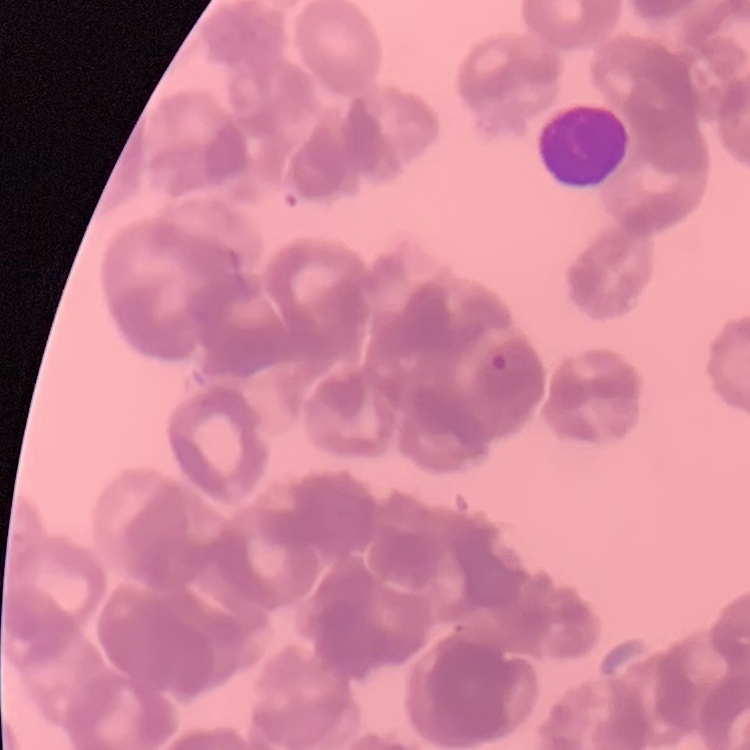

Summary:
  - Red blood cell morphology: rouleaux formation
  - Preparation: thin peripheral smear
  - Stain: Field's or Giemsa
  - Image type: one tile cut from a larger photomicrograph